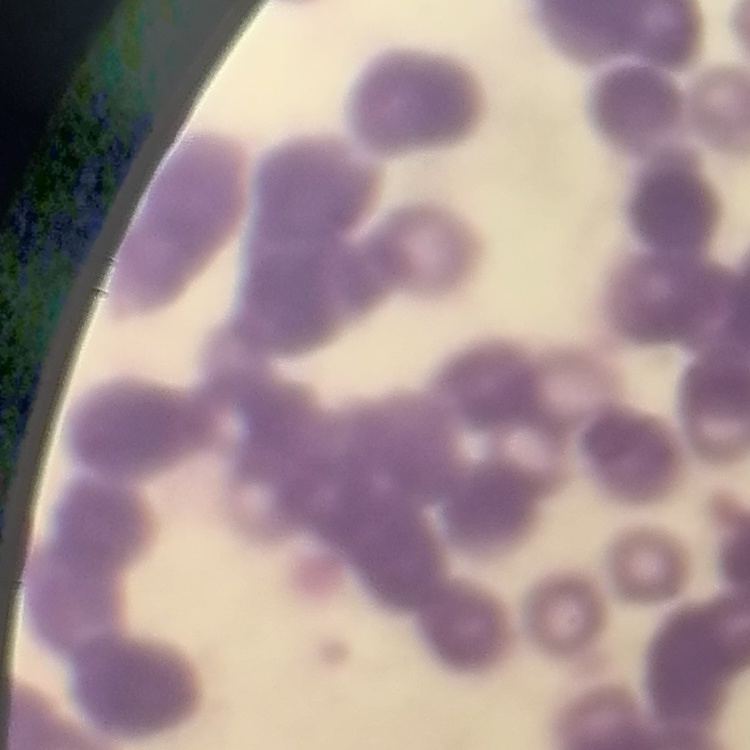

The erythrocytes exhibit rouleaux formation. Thin peripheral smear. Stained with either Field's or Giemsa. Square crop of a larger photomicrograph.